Report the malaria status of this cell.
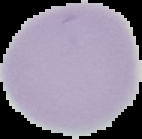

Uninfected.

From a thin blood film. Cell region segmented out of the field of view; the surrounding area is masked to black. Image is 142×139 pixels.